Report the malaria status of this cell.
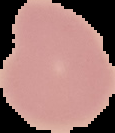
It is uninfected.

Summary:
  - Image type: segmented cell region on a black background
  - Image size: 115×133 pixels
  - Preparation: thin blood smear